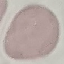
malaria status = uninfected
preparation = thin blood smear
stain = Giemsa
capture = smartphone camera at the microscope eyepiece
image type = cell patch, automatically extracted from a larger field of view and resized to 64 × 64 pixels